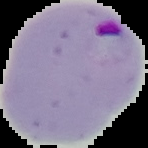

result = Plasmodium parasites detected
image type = segmented cell region on a black background
preparation = thin blood film
image size = 148×148 pixels